Identify the parasite.
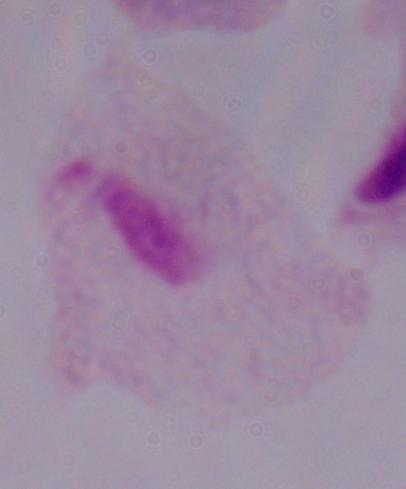

A trichomonad.

Photomicrograph. 1000x magnification.